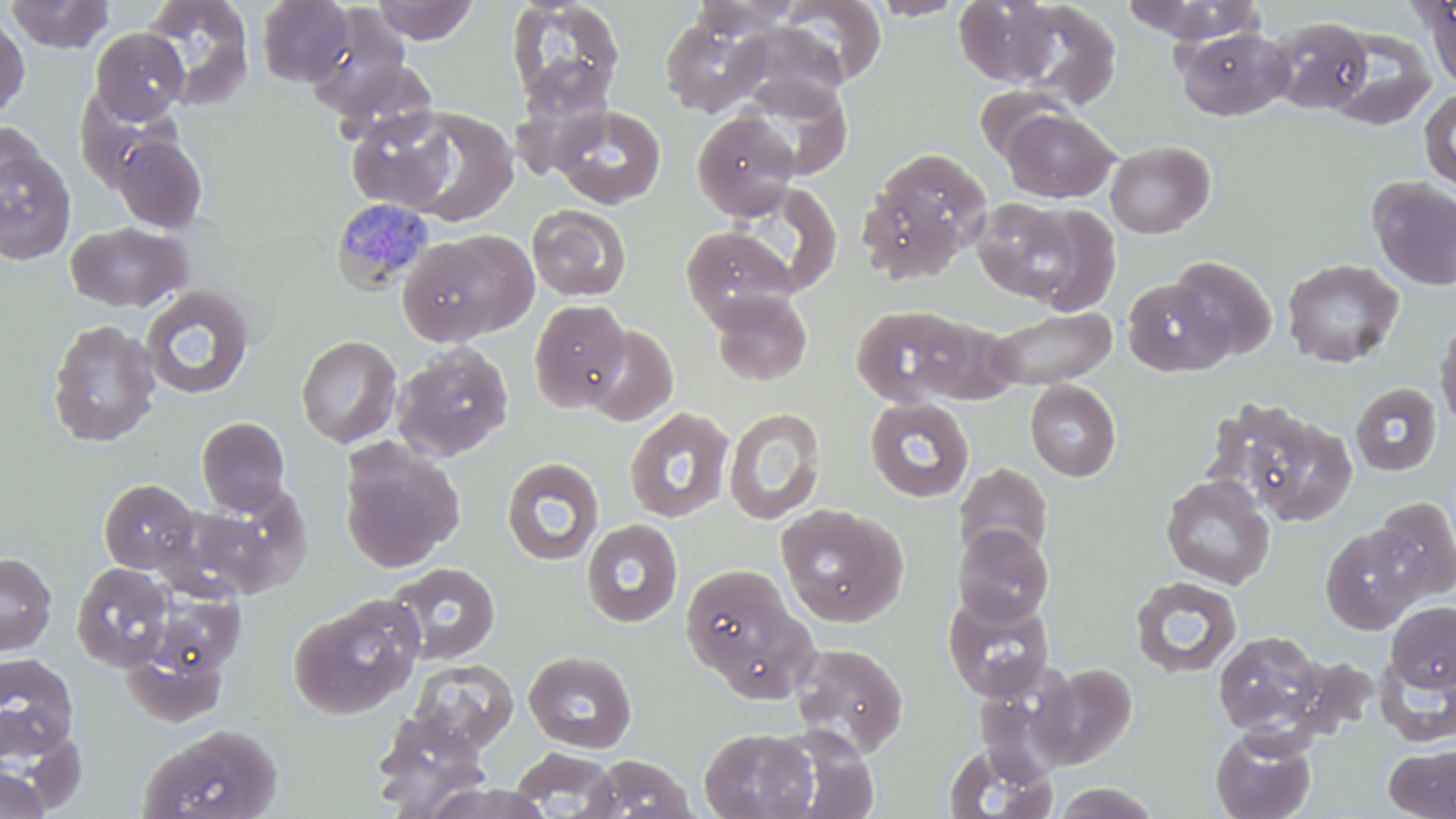 Approximate bounding boxes as [x1, y1, x2, y2] in pixels. Plasmodium malariae-infected red blood cell locations: [331, 196, 437, 296]. Uninfected red blood cell locations: [3, 0, 115, 54], [139, 0, 255, 111], [256, 0, 355, 87], [372, 0, 477, 44], [505, 0, 625, 114], [688, 0, 802, 38], [778, 0, 887, 87], [867, 0, 969, 20], [954, 0, 1060, 86], [1008, 1, 1121, 108], [1122, 1, 1265, 45], [1416, 1, 1456, 91], [304, 7, 414, 119], [0, 11, 30, 118], [661, 16, 767, 117], [1266, 16, 1375, 116], [729, 21, 850, 114], [1174, 26, 1294, 120], [1325, 26, 1438, 130], [90, 27, 189, 123], [736, 73, 854, 181], [975, 83, 1078, 166], [1419, 88, 1456, 192], [550, 104, 666, 209], [393, 106, 519, 226], [346, 108, 458, 212], [1001, 108, 1118, 203], [692, 111, 799, 220], [0, 120, 44, 205], [112, 134, 208, 233], [1105, 140, 1215, 238], [863, 148, 992, 277], [0, 149, 77, 264], [1367, 177, 1456, 290], [970, 198, 1085, 304], [527, 204, 632, 301], [64, 221, 192, 312], [681, 225, 798, 328], [397, 230, 534, 345], [1168, 255, 1277, 362], [1282, 258, 1404, 368], [1122, 278, 1231, 376], [139, 285, 256, 400], [708, 289, 813, 387], [529, 299, 631, 412], [850, 304, 975, 407], [984, 305, 1118, 390], [1433, 315, 1456, 433], [47, 318, 161, 447], [581, 323, 679, 427], [296, 334, 402, 448], [392, 343, 514, 462], [1025, 380, 1122, 481], [1350, 382, 1442, 477], [863, 396, 975, 503], [1212, 398, 1354, 525], [624, 407, 735, 523], [723, 407, 826, 525], [197, 416, 290, 515], [339, 442, 464, 573], [501, 456, 604, 566], [953, 463, 1053, 568], [1160, 474, 1276, 589], [99, 478, 201, 575], [178, 491, 310, 600], [1371, 497, 1456, 602], [775, 503, 908, 627], [581, 519, 684, 628], [953, 525, 1054, 626], [1320, 525, 1424, 634], [0, 552, 57, 655], [386, 561, 501, 665], [71, 562, 175, 671], [680, 563, 813, 696], [147, 576, 243, 678], [1129, 576, 1243, 677], [942, 591, 1055, 701], [288, 596, 423, 720], [1386, 601, 1456, 692], [125, 615, 229, 723], [1213, 630, 1328, 739], [790, 642, 908, 756], [524, 650, 637, 753], [1373, 652, 1456, 748], [0, 653, 79, 761], [408, 660, 518, 752], [1038, 663, 1137, 766], [371, 711, 490, 814], [138, 723, 284, 819], [1210, 726, 1317, 819], [699, 727, 818, 819], [767, 727, 880, 819], [2, 738, 72, 814], [941, 741, 1058, 819], [1384, 742, 1456, 818], [509, 747, 619, 817], [585, 753, 697, 818], [0, 766, 53, 819], [1048, 782, 1162, 819], [422, 783, 555, 819]. Slide-level diagnosis: Plasmodium malariae. Single field of view. Light microscopy. May-Grünwald-Giemsa-stained preparation. Thin blood film. Image is 1456×819 pixels. Captured at 1000x magnification.